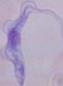

A trypanosome is shown. Photomicrograph. 1000x magnification.